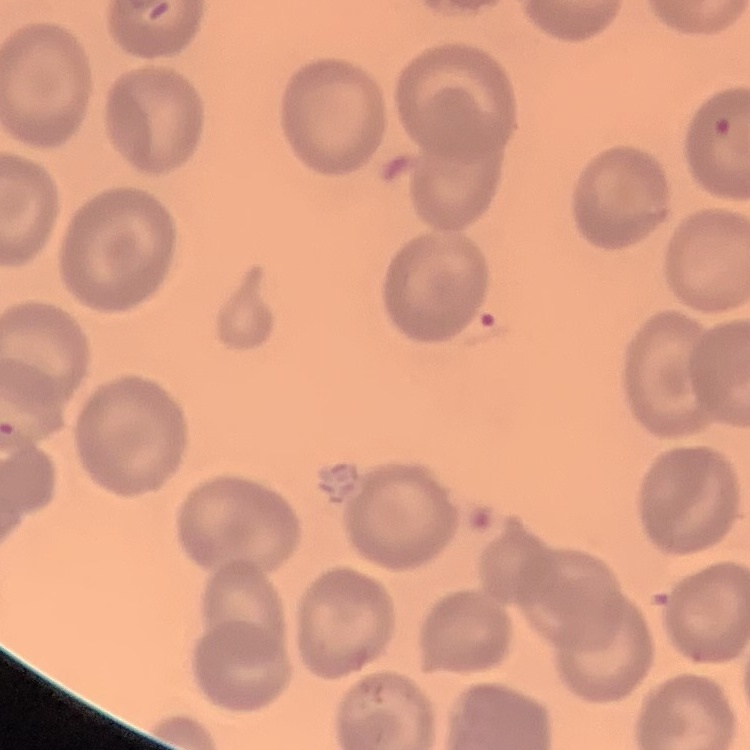
red_blood_cell_morphology: no rouleaux formation
preparation: thin blood film
image_type: square crop of a larger photomicrograph
stain: Field's or Giemsa